Name the cell type shown.
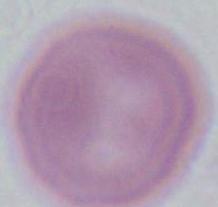

An erythrocyte.

Captured at 1000x magnification. Micrograph.